Report the malaria status of this cell.
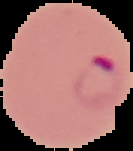
It is parasitized.

preparation = thin blood film
image size = 133×151 pixels
image type = cell region segmented out of the field of view; surrounding area masked to black